Describe the morphology of the red blood cells.
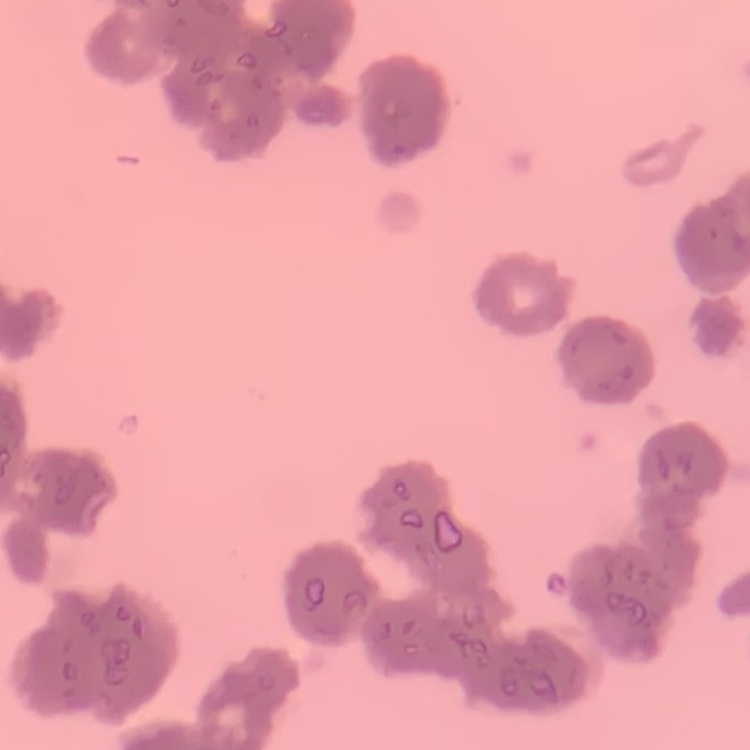
Rouleaux formation.

Square crop of a larger photomicrograph. Thin blood smear. Field's or Giemsa stain.